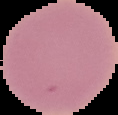
Summary:
  - Image type: segmented cell region with the area outside set to black
  - Image size: 118×115 pixels
  - Preparation: thin blood film
  - Result: negative for Plasmodium parasites